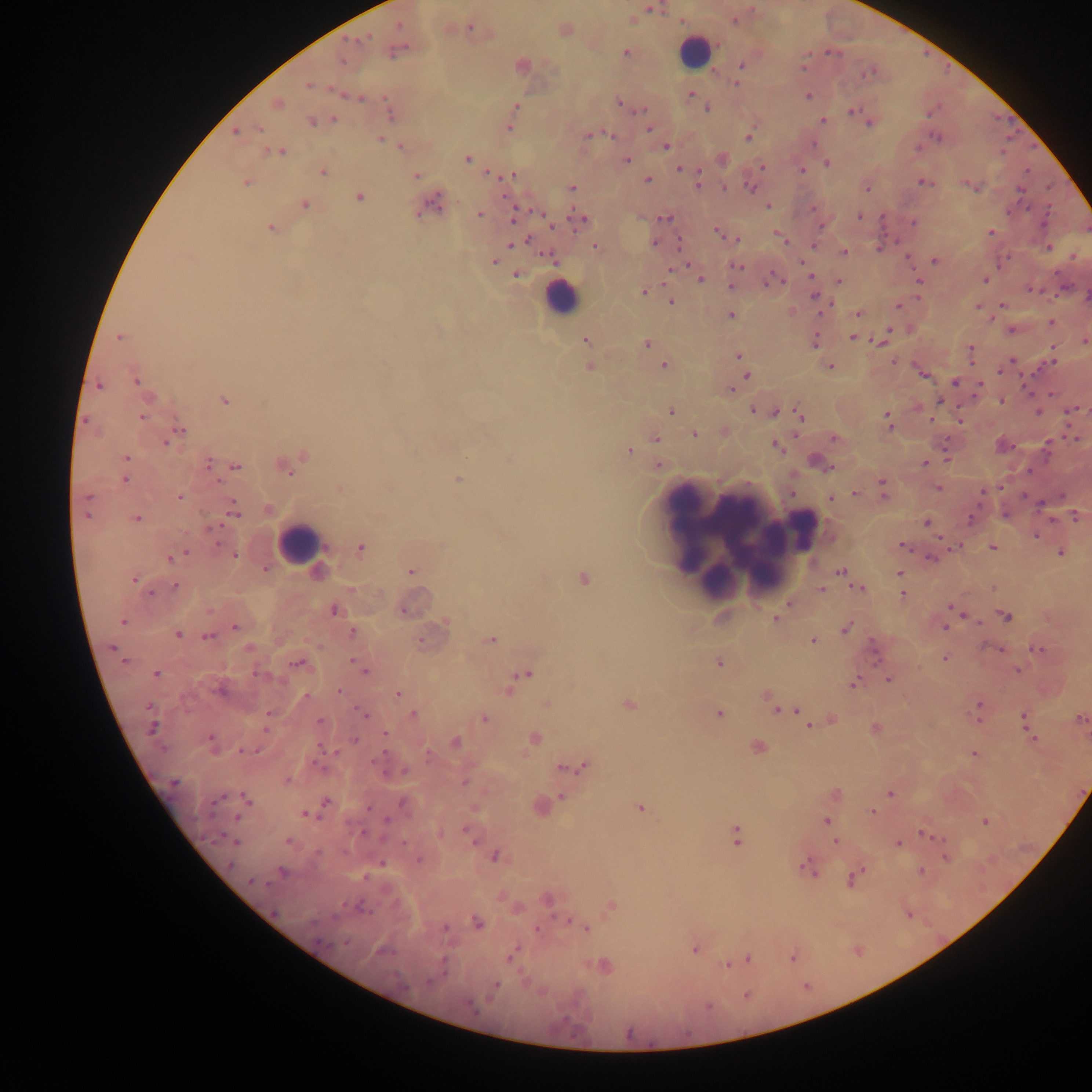

Approximate centers as {x, y} in pixels.
Summary:
  - Malaria parasite locations: {650, 9}, {680, 22}, {469, 27}, {367, 36}, {352, 40}, {359, 40}, {625, 51}, {827, 51}, {808, 52}, {343, 61}, {741, 64}, {802, 67}, {735, 83}, {308, 86}, {690, 94}, {808, 96}, {359, 98}, {619, 102}, {706, 106}, {516, 107}, {643, 110}, {851, 110}, {933, 111}, {638, 112}, {929, 114}, {332, 119}, {821, 119}, {310, 121}, {868, 123}, {509, 128}, {259, 129}, {649, 129}, {235, 133}, {610, 134}, {587, 135}, {936, 137}, {379, 138}, {747, 138}, {665, 145}, {918, 146}, {279, 153}, {1002, 153}, {468, 159}, {626, 160}, {828, 163}, {761, 166}, {678, 169}, {802, 170}, {1026, 170}, {488, 172}, {699, 173}, {322, 174}, {416, 176}, {513, 176}, {647, 180}, {921, 181}, {963, 182}, {247, 183}, {698, 184}, {751, 186}, {974, 186}, {572, 187}, {726, 187}, {867, 187}, {1018, 191}, {359, 196}, {305, 205}, {768, 206}, {1029, 207}, {813, 208}, {1047, 210}, {418, 212}, {1008, 212}, {480, 213}, {540, 213}, {572, 214}, {859, 216}, {663, 218}, {883, 219}, {512, 221}, {575, 221}, {914, 222}, {269, 227}, {822, 227}, {550, 228}, {991, 231}, {717, 232}, {528, 240}, {897, 241}, {655, 242}, {677, 242}, {508, 244}, {595, 245}, {813, 245}, {879, 247}, {1048, 247}, {845, 252}, {542, 255}, {908, 256}, {1074, 257}, {494, 261}, {800, 261}, {934, 261}, {738, 266}, {771, 273}, {515, 275}, {811, 277}, {701, 280}, {783, 281}, {838, 281}, {986, 281}, {767, 282}, {918, 282}, {730, 284}, {1029, 289}, {1042, 289}, {643, 291}, {1058, 294}, {814, 296}, {1054, 297}, {671, 302}, {833, 304}, {1000, 304}, {897, 305}, {977, 305}, {731, 314}, {821, 314}, {856, 315}, {991, 320}, {1051, 323}, {890, 330}, {1011, 330}, {119, 337}, {852, 337}, {867, 338}, {873, 340}, {1084, 341}, {646, 342}, {880, 343}, {972, 346}, {1053, 347}, {741, 356}, {1014, 360}, {1054, 361}, {894, 362}, {663, 364}, {972, 364}, {830, 366}, {999, 371}, {746, 375}, {923, 375}, {1022, 379}, {136, 381}, {954, 383}, {98, 385}, {980, 385}, {735, 386}, {730, 390}, {1050, 394}, {940, 399}, {224, 401}, {1000, 401}, {1081, 409}, {1085, 409}, {753, 410}, {1072, 410}, {671, 411}, {1038, 412}, {775, 413}, {799, 414}, {885, 414}, {1067, 417}, {85, 419}, {142, 419}, {931, 420}, {960, 421}, {890, 427}, {179, 429}, {694, 434}, {795, 434}, {656, 438}, {1074, 439}, {832, 440}, {1049, 440}, {167, 444}, {630, 450}, {127, 457}, {946, 460}, {208, 461}, {924, 462}, {235, 467}, {1029, 469}, {292, 473}, {126, 480}, {217, 481}, {883, 483}, {937, 487}, {1000, 487}, {883, 492}, {981, 493}, {854, 494}, {1024, 495}, {87, 496}, {180, 497}, {832, 498}, {1041, 503}, {233, 510}, {85, 515}, {1075, 516}, {139, 518}, {971, 520}, {1052, 520}, {926, 522}, {222, 524}, {207, 529}, {1034, 535}, {938, 538}, {218, 542}, {900, 544}, {360, 547}, {959, 547}, {993, 548}, {186, 551}, {1060, 552}, {235, 556}, {168, 558}, {928, 558}, {840, 571}, {411, 572}, {898, 573}, {134, 579}, {174, 584}, {857, 587}, {822, 590}, {152, 593}, {904, 593}, {788, 603}, {949, 605}, {335, 611}, {402, 611}, {965, 616}, {1004, 617}, {773, 619}, {980, 621}, {235, 626}, {944, 627}, {846, 629}, {179, 633}, {206, 637}, {419, 638}, {812, 639}, {248, 647}, {111, 648}, {1040, 649}, {1000, 651}, {946, 658}, {351, 660}, {296, 662}, {718, 662}, {1018, 671}, {364, 672}, {156, 673}, {256, 673}, {522, 675}, {890, 678}, {852, 683}, {507, 690}, {337, 692}, {399, 693}, {307, 696}, {767, 696}, {629, 704}, {977, 705}, {776, 709}, {795, 710}, {268, 713}, {361, 713}, {718, 713}, {413, 714}, {1022, 715}, {365, 716}, {484, 718}, {319, 719}, {1080, 719}, {978, 720}, {809, 726}, {267, 729}, {385, 732}, {210, 737}, {354, 739}, {1032, 739}, {534, 741}, {320, 747}, {241, 751}, {334, 751}, {384, 753}, {428, 754}, {974, 754}, {372, 759}, {319, 766}, {560, 767}, {581, 767}, {404, 770}, {287, 781}, {464, 783}, {890, 795}, {561, 796}, {218, 798}, {368, 808}, {871, 812}, {304, 814}, {386, 820}, {826, 821}, {986, 823}, {464, 829}, {920, 832}, {362, 834}, {735, 836}, {220, 837}, {943, 839}, {288, 841}, {474, 841}, {896, 842}, {403, 843}, {835, 843}, {317, 853}, {496, 856}, {946, 857}, {229, 864}, {382, 864}, {802, 864}, {862, 870}, {920, 870}, {364, 878}, {850, 880}, {250, 882}, {268, 884}, {568, 919}, {478, 922}, {444, 927}, {535, 928}, {587, 929}, {344, 944}, {693, 949}, {509, 958}, {747, 959}, {726, 965}, {443, 974}, {496, 985}, {745, 995}, {706, 1006}
  - Leukocyte locations: {696, 49}, {560, 297}, {734, 509}, {686, 526}, {807, 528}, {300, 544}, {765, 563}, {721, 587}
  - Field of view: single
  - Image size: 1092×1092 pixels
  - Preparation: thick blood smear
  - Country: Ghana
  - Capture: mobile-phone photograph through a microscope